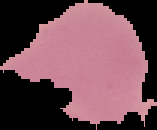

result = negative for Plasmodium parasites
image size = 157×130 pixels
image type = cell region segmented out of the field of view; surrounding area masked to black
preparation = thin blood film